Comment on the morphology of the red blood cells.
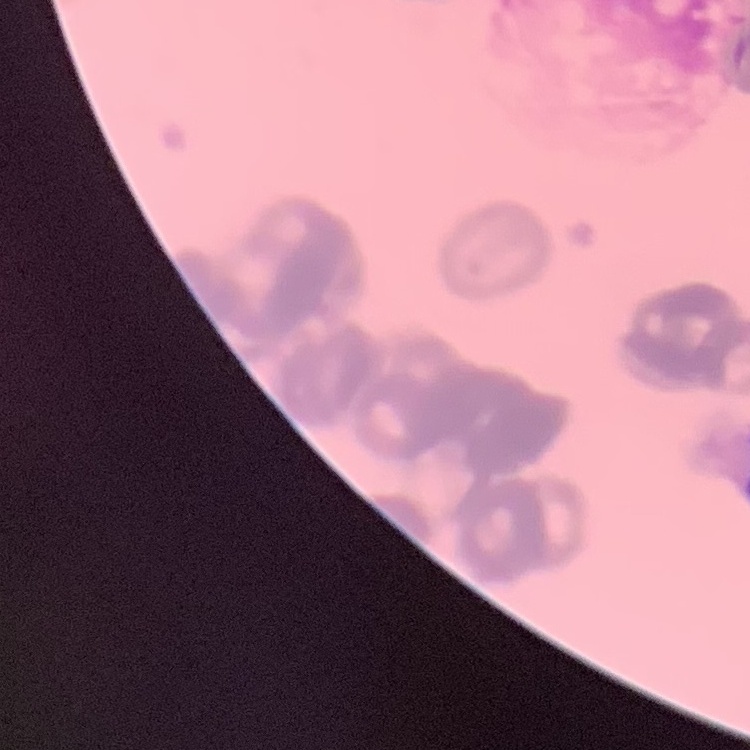

Rouleaux formation.

Summary:
  - Preparation: thin blood smear
  - Stain: Field's or Giemsa
  - Image type: one tile cut from a larger photomicrograph